Describe the morphology of the red blood cells.
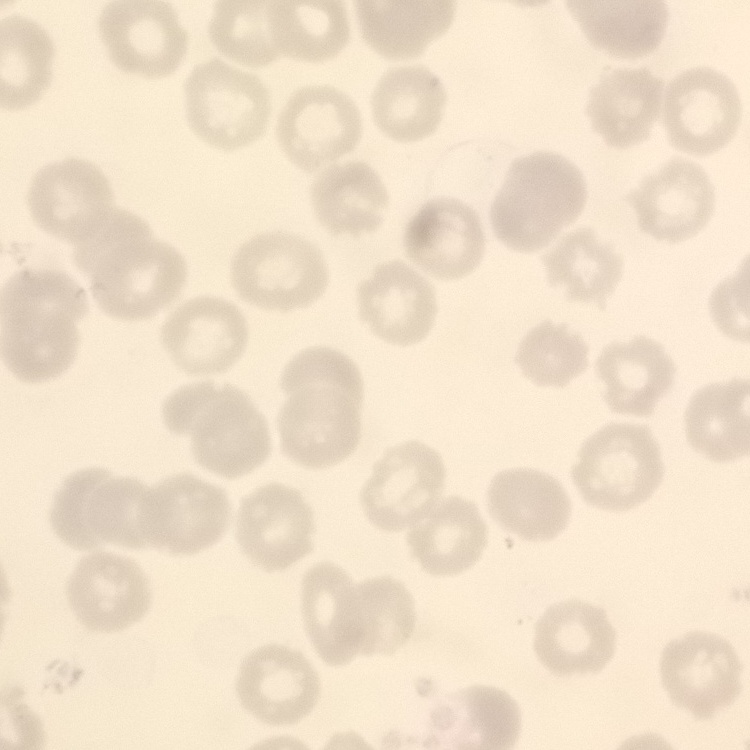
No rouleaux formation.

image_type: one tile cut from a larger photomicrograph
preparation: thin blood film
stain: Field's or Giemsa